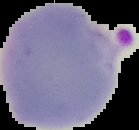
Summary:
  - Preparation: thin blood film
  - Result: malaria parasites identified
  - Image size: 139×130 pixels
  - Image type: segmented cell region on a black background